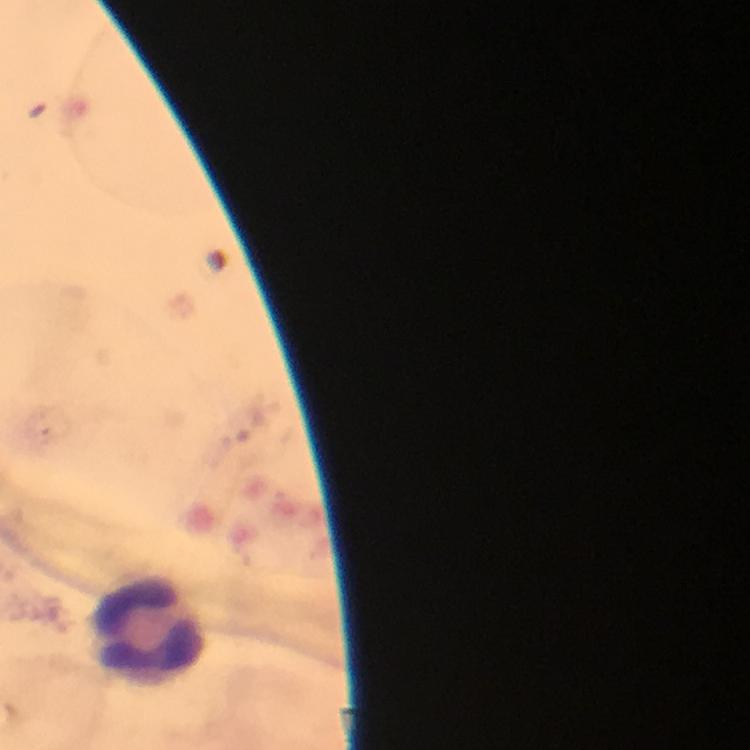

Approximate centers as {x, y} in pixels.
Summary:
  - Leukocyte locations: {145, 629}
  - Stain: Giemsa
  - Magnification: 100x
  - Preparation: thick smear
  - Malaria parasites: none detected
  - Context: from a malaria diagnostic workup
  - Capture: smartphone photograph through a microscope
  - Image size: 750×750 pixels
  - Cropped from: a single field of view
  - Immersion oil: used